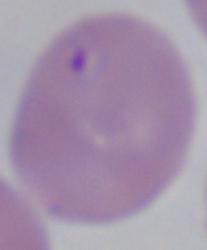

A Babesia parasite is seen. 1000x magnification. Micrograph.